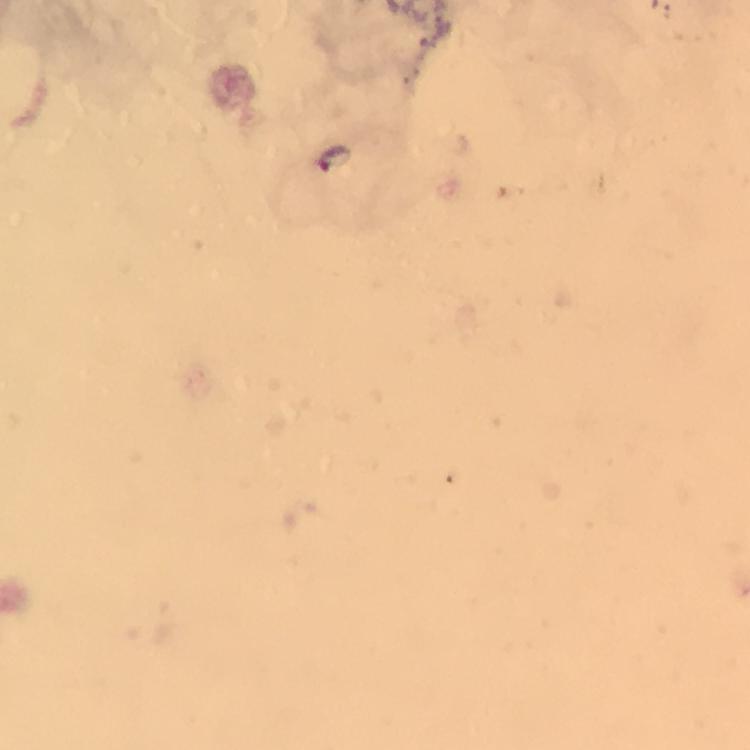
Approximate centers as {x, y} in pixels. Malaria parasite locations: {335, 161}. Cropped region of a single field of view. Smartphone photograph taken through a microscope. Image is 750×750 pixels. Immersion oil was used. Thick blood film. From a malaria diagnostic workup. At 100x magnification. Giemsa-stained preparation.